Name the parasite shown.
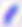
This is Toxoplasma gondii.

modality = micrograph
magnification = 400x